Report the malaria status of this cell.
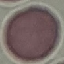
It is uninfected.

Thin blood smear. Cell patch, automatically extracted from a larger field of view and resized to 64 × 64 pixels. Giemsa stain. Photographed with a smartphone camera at the microscope eyepiece.